State which parasite is depicted.
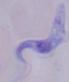

A trypanosome.

magnification = 1000x
modality = micrograph